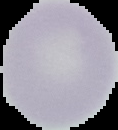

Summary:
  - Image size: 118×130 pixels
  - Preparation: thin blood smear
  - Image type: segmented cell region with the area outside set to black
  - Malaria status: uninfected